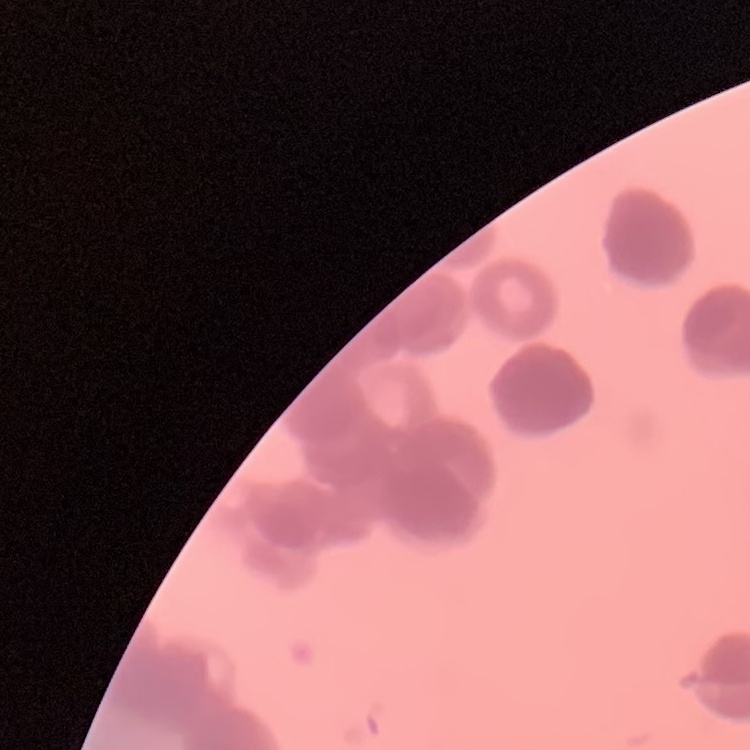
Summary:
  - Erythrocyte morphology: rouleaux formation
  - Stain: Field's or Giemsa
  - Image type: square crop of a larger photomicrograph
  - Preparation: thin blood film